Outline each blood parasite and name the species.
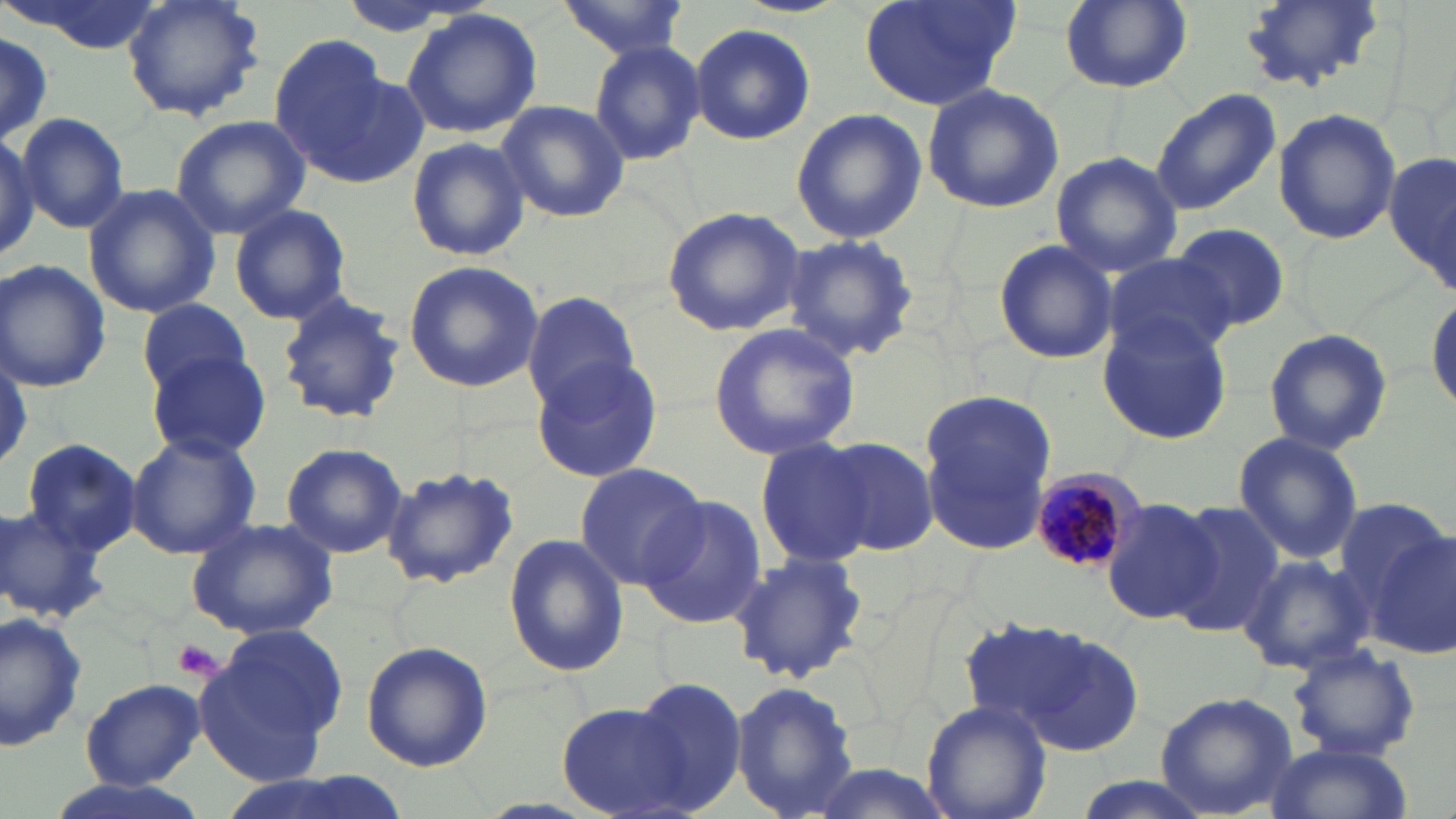
Approximate bounding boxes as [x1, y1, x2, y2] in pixels.
Plasmodium malariae-infected red blood cells: [1024, 471, 1142, 578].
No Plasmodium falciparum, Plasmodium ovale, Plasmodium vivax, Babesia divergens, or Trypanosoma brucei observed.

Uninfected red blood cell locations: [3, 0, 167, 54], [120, 0, 266, 123], [557, 0, 694, 58], [856, 0, 1021, 111], [1057, 0, 1194, 95], [1238, 0, 1387, 94], [401, 8, 543, 138], [691, 22, 815, 145], [0, 35, 56, 142], [267, 36, 410, 183], [586, 39, 707, 167], [921, 83, 1065, 213], [1150, 88, 1281, 214], [494, 99, 629, 224], [791, 107, 926, 246], [1273, 109, 1402, 247], [17, 113, 130, 233], [170, 115, 310, 239], [0, 131, 40, 266], [405, 136, 529, 263], [1050, 151, 1182, 276], [1386, 152, 1454, 285], [83, 184, 220, 320], [228, 203, 352, 326], [661, 204, 810, 337], [1172, 225, 1288, 331], [782, 234, 921, 363], [991, 239, 1118, 365], [1102, 255, 1237, 361], [0, 259, 112, 394], [402, 261, 545, 394], [1428, 289, 1456, 415], [521, 291, 642, 412], [275, 292, 406, 428], [136, 299, 254, 399], [1098, 316, 1233, 446], [708, 322, 860, 461], [1263, 328, 1393, 455], [149, 351, 272, 461], [530, 355, 664, 486], [917, 389, 1060, 556], [124, 428, 261, 558], [1233, 431, 1363, 565], [822, 436, 940, 556], [754, 438, 877, 570], [23, 439, 144, 554], [279, 442, 408, 559], [377, 462, 523, 589], [573, 463, 710, 589], [639, 496, 765, 631], [1101, 497, 1218, 626], [1163, 502, 1284, 640], [0, 503, 109, 624], [186, 517, 339, 641], [1364, 521, 1456, 660], [503, 533, 630, 678], [724, 551, 871, 686], [1237, 554, 1374, 675], [0, 609, 91, 753], [976, 619, 1148, 756], [198, 626, 346, 784], [360, 641, 493, 772], [1285, 642, 1422, 761], [624, 676, 749, 812], [78, 679, 205, 788], [730, 680, 861, 819], [1155, 693, 1297, 817], [922, 700, 1051, 819], [557, 702, 699, 819], [1259, 739, 1412, 819], [804, 760, 957, 819], [34, 772, 213, 819], [212, 774, 420, 819]. Platelet locations: [171, 639, 224, 681]. Slide-level diagnosis: Plasmodium malariae. Image is 1456×819 pixels. Single field of view. Thin blood film. May-Grünwald-Giemsa stain. Optical microscopy. 1000x magnification.